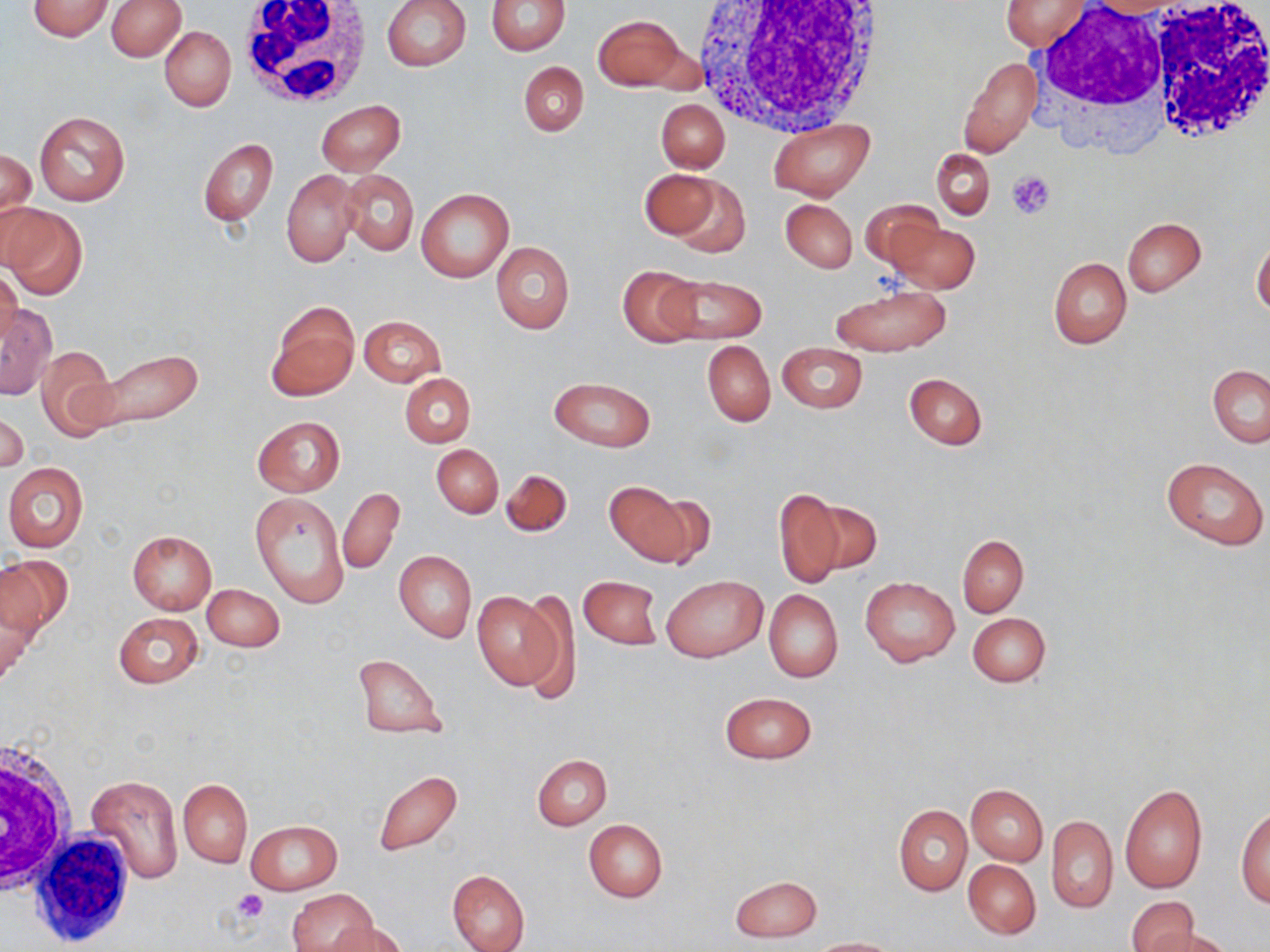

slide-level diagnosis = negative for blood parasites
platelet locations = approximate bounding boxes as [x1, y1, x2, y2] in pixels: [1008, 171, 1053, 220], [232, 888, 270, 923]
image size = 1270×952 pixels
stain = May-Grünwald-Giemsa
uninfected red blood cell locations = approximate bounding boxes as [x1, y1, x2, y2] in pixels: [26, 0, 114, 41], [107, 0, 186, 61], [382, 0, 471, 70], [487, 0, 570, 54], [1001, 1, 1088, 50], [594, 15, 687, 90], [160, 25, 235, 111], [958, 58, 1040, 158], [517, 61, 589, 136], [656, 99, 730, 173], [317, 100, 405, 175], [34, 110, 130, 206], [768, 120, 873, 200], [199, 137, 278, 225], [1, 149, 36, 240], [931, 149, 994, 220], [639, 168, 720, 239], [340, 169, 418, 255], [282, 170, 359, 267], [662, 174, 749, 257], [415, 188, 513, 281], [781, 199, 857, 272], [861, 200, 946, 273], [1, 204, 87, 300], [1122, 217, 1206, 297], [886, 220, 981, 293], [1252, 239, 1270, 317], [491, 242, 575, 333], [1049, 258, 1132, 350], [618, 266, 703, 347], [0, 267, 23, 347], [658, 272, 767, 345], [830, 284, 952, 356], [266, 301, 359, 401], [0, 303, 57, 398], [358, 315, 445, 387], [702, 340, 774, 426], [777, 342, 866, 414], [36, 345, 117, 439], [92, 349, 203, 432], [1208, 365, 1270, 447], [401, 373, 476, 447], [904, 373, 988, 450], [549, 377, 655, 451], [0, 412, 27, 474], [252, 416, 345, 497], [432, 444, 503, 518], [1161, 457, 1268, 550], [2, 464, 89, 551], [501, 469, 572, 538], [605, 481, 700, 566], [338, 487, 404, 574], [774, 488, 846, 587], [644, 489, 718, 570], [249, 490, 350, 608], [806, 498, 881, 577], [127, 530, 217, 613], [957, 534, 1028, 616], [144, 548, 244, 629], [394, 550, 476, 642], [0, 554, 66, 665], [578, 575, 662, 649], [663, 575, 767, 662], [860, 577, 960, 666], [202, 583, 284, 651], [472, 589, 562, 689], [764, 589, 843, 682], [515, 591, 578, 703], [114, 611, 202, 689], [968, 611, 1051, 687], [352, 654, 446, 739], [719, 691, 817, 764], [533, 755, 612, 829], [372, 769, 462, 856], [85, 775, 184, 884], [178, 779, 252, 867], [966, 784, 1048, 865], [1120, 784, 1207, 893], [893, 805, 971, 895], [1236, 805, 1269, 908], [1046, 815, 1118, 913], [583, 819, 668, 902], [246, 820, 341, 893], [963, 859, 1041, 938], [447, 870, 529, 952], [728, 875, 822, 942], [290, 888, 378, 952], [1126, 896, 1199, 952], [329, 921, 410, 952], [1146, 928, 1231, 952], [808, 937, 898, 951]
field of view = one of a larger specimen
magnification = 1000x
modality = light microscopy
white blood cell locations = approximate bounding boxes as [x1, y1, x2, y2] in pixels: [235, 0, 373, 109], [691, 0, 889, 135], [1140, 2, 1270, 148], [1032, 5, 1181, 132], [0, 733, 78, 898], [36, 825, 141, 949]
preparation = thin blood smear